Name the blood parasite species.
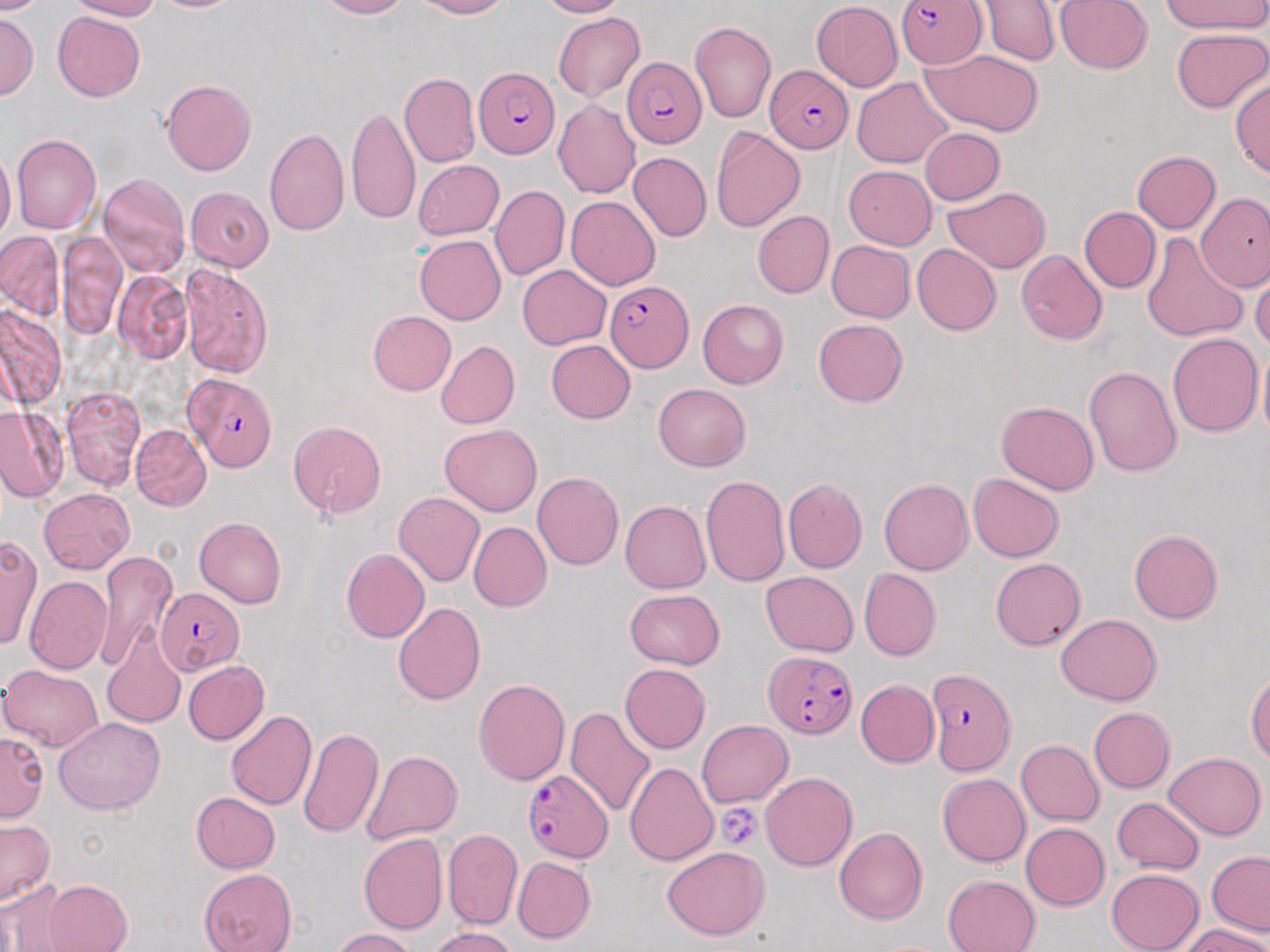

Plasmodium falciparum.

Summary:
  - Coordinate format: approximate bounding boxes as [x1, y1, x2, y2] in pixels
  - Plasmodium falciparum-infected red blood cell locations: [897, 0, 986, 69], [622, 56, 706, 147], [764, 64, 854, 154], [474, 66, 558, 158], [605, 280, 692, 375], [183, 372, 276, 472], [155, 588, 244, 675], [767, 651, 857, 736], [925, 668, 1015, 776], [522, 768, 613, 863]
  - Uninfected red blood cell locations: [0, 0, 53, 14], [67, 0, 161, 20], [152, 0, 244, 12], [319, 0, 411, 19], [415, 0, 511, 19], [536, 0, 625, 18], [979, 0, 1061, 66], [1053, 0, 1154, 75], [1163, 0, 1269, 35], [812, 1, 903, 90], [52, 12, 145, 102], [553, 12, 645, 102], [0, 13, 38, 99], [690, 20, 776, 123], [1170, 28, 1269, 113], [920, 48, 1046, 136], [400, 73, 480, 168], [851, 77, 951, 168], [1229, 78, 1270, 180], [161, 79, 256, 175], [553, 98, 641, 199], [347, 103, 419, 226], [264, 127, 349, 237], [711, 127, 805, 232], [919, 127, 1005, 206], [12, 135, 101, 235], [0, 149, 16, 246], [628, 151, 711, 242], [1132, 151, 1220, 234], [412, 160, 504, 240], [844, 166, 936, 249], [98, 173, 190, 277], [490, 184, 570, 281], [942, 185, 1049, 273], [186, 186, 275, 271], [1197, 193, 1270, 291], [566, 196, 660, 290], [1079, 206, 1160, 293], [753, 211, 834, 297], [1, 231, 64, 319], [1141, 232, 1247, 343], [57, 233, 126, 339], [414, 236, 507, 325], [826, 240, 916, 323], [912, 243, 1001, 336], [1015, 250, 1107, 344], [180, 264, 273, 379], [517, 265, 611, 350], [1250, 268, 1270, 352], [113, 271, 193, 365], [697, 299, 788, 389], [0, 305, 65, 411], [367, 310, 457, 396], [814, 318, 908, 406], [1167, 333, 1263, 437], [546, 339, 636, 423], [435, 340, 520, 430], [1257, 340, 1269, 448], [1083, 366, 1182, 477], [654, 383, 750, 470], [61, 385, 146, 490], [996, 400, 1099, 494], [0, 409, 67, 502], [289, 421, 386, 518], [131, 424, 210, 511], [440, 424, 541, 517], [532, 472, 623, 570], [968, 473, 1064, 562], [700, 474, 790, 589], [782, 478, 867, 573], [878, 478, 972, 575], [39, 487, 135, 574], [394, 492, 485, 587], [620, 500, 710, 593], [194, 517, 287, 608], [468, 522, 552, 612], [1129, 529, 1223, 624], [0, 534, 41, 653], [341, 549, 429, 642], [94, 551, 177, 672], [991, 557, 1086, 650], [859, 568, 942, 660], [761, 571, 858, 657], [24, 576, 113, 674], [624, 589, 725, 669], [393, 603, 486, 706], [1055, 614, 1161, 705], [102, 632, 186, 728], [183, 661, 269, 745], [619, 663, 710, 753], [1, 664, 104, 752], [1247, 674, 1270, 766], [474, 677, 570, 785], [855, 679, 939, 768], [566, 706, 657, 819], [1088, 707, 1174, 794], [226, 710, 317, 810], [54, 717, 165, 814], [698, 719, 792, 807], [298, 727, 384, 839], [0, 731, 48, 823], [1016, 739, 1104, 826], [361, 749, 463, 845], [1163, 752, 1267, 840], [625, 762, 718, 866], [761, 773, 857, 871], [937, 774, 1030, 867], [191, 792, 280, 873], [1113, 797, 1204, 875], [0, 819, 55, 907], [1021, 823, 1110, 911], [834, 827, 927, 925], [443, 829, 523, 930], [358, 833, 448, 934], [662, 846, 769, 940], [1206, 851, 1270, 936], [512, 856, 596, 944], [199, 868, 297, 952], [1105, 868, 1203, 952], [943, 874, 1041, 952], [41, 880, 132, 951], [0, 881, 75, 951], [1181, 925, 1270, 952], [431, 926, 517, 952], [330, 928, 418, 952]
  - Platelet locations: [715, 803, 765, 849]
  - Preparation: thin blood film
  - Stain: May-Grünwald-Giemsa
  - Image size: 1270×952 pixels
  - Field of view: single
  - Modality: optical microscopy
  - Magnification: 1000x